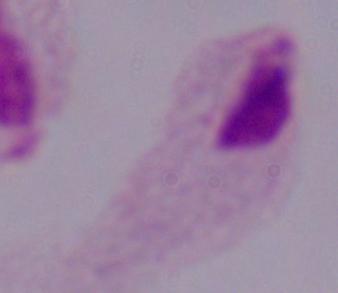

{
  "modality": "micrograph",
  "identification": "trichomonad",
  "magnification": "1000x"
}